Report the malaria status of this cell.
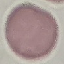

Uninfected.

{
  "image_type": "automatically extracted cell patch, resized to 64 × 64 pixels",
  "preparation": "thin blood smear",
  "capture": "smartphone through the microscope eyepiece",
  "stain": "Giemsa"
}